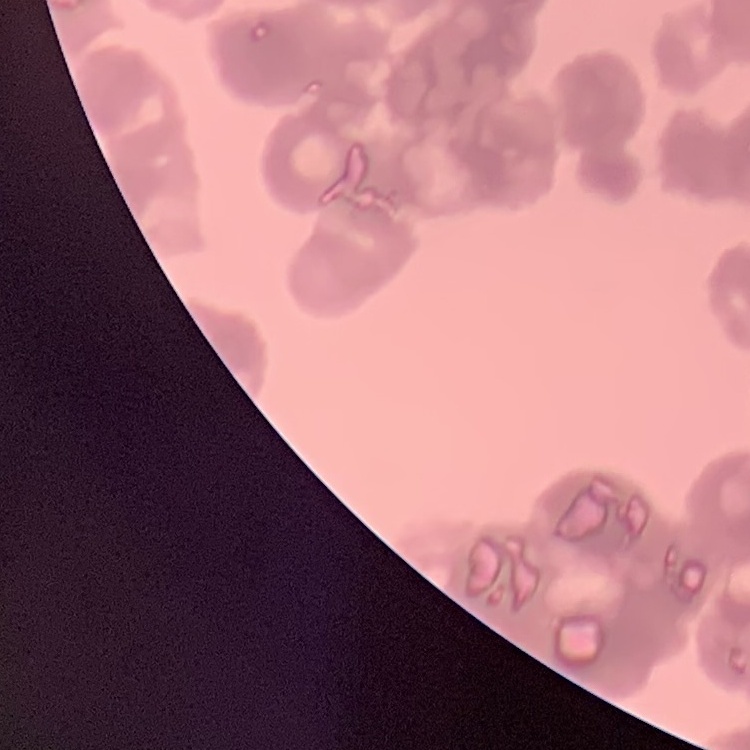

red blood cell morphology = rouleaux formation
stain = Field's or Giemsa
image type = one tile cut from a larger photomicrograph
preparation = thin blood film